Point out each Plasmodium parasite.
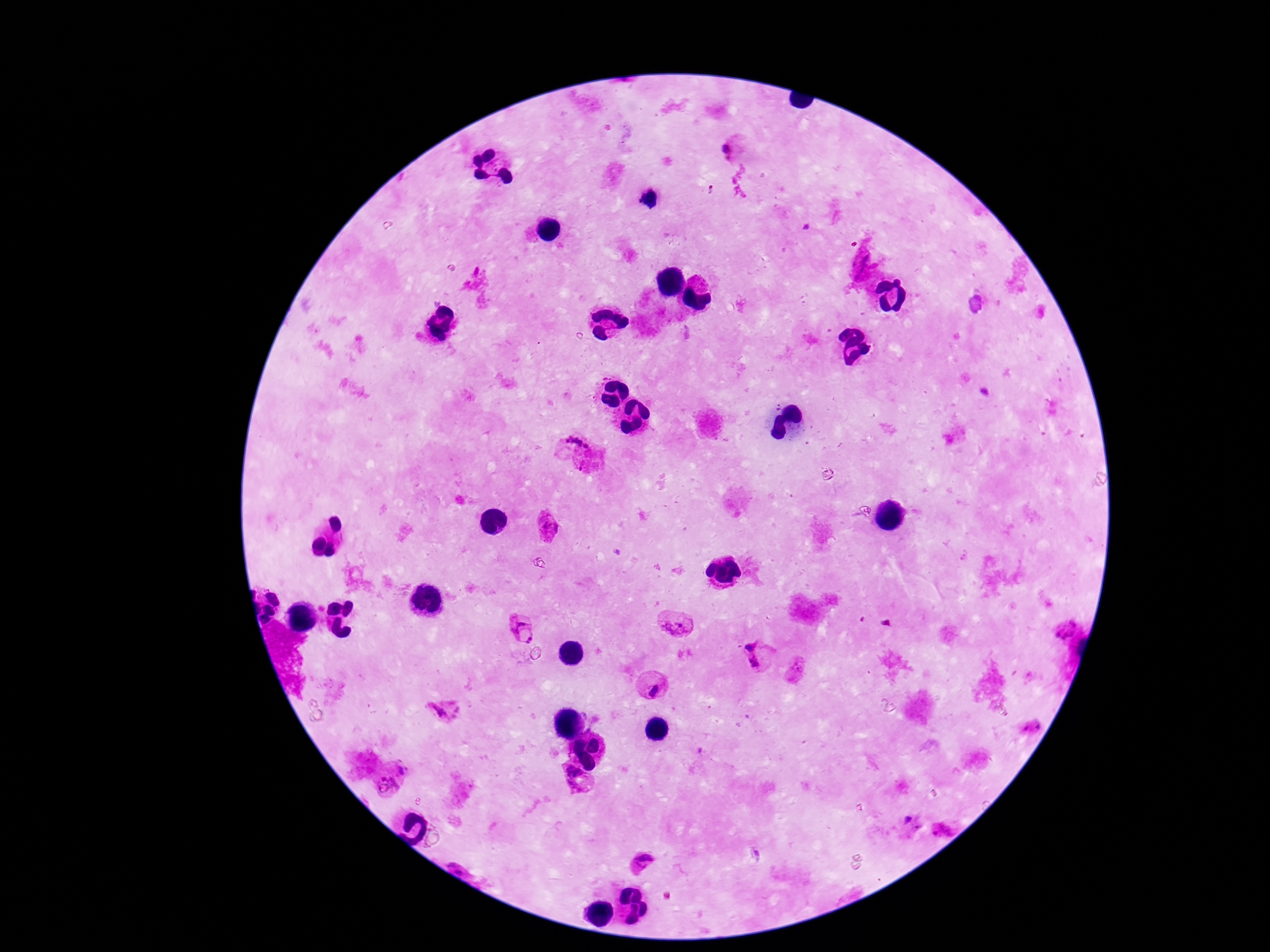
Approximate object centers, in pixels from the top-left corner.
Plasmodium parasites: (x=728, y=149), (x=571, y=438), (x=588, y=447), (x=546, y=527), (x=678, y=623), (x=522, y=629), (x=752, y=645), (x=755, y=661), (x=651, y=685), (x=442, y=711), (x=1033, y=727), (x=400, y=771), (x=574, y=780), (x=909, y=820), (x=944, y=829), (x=643, y=863).

field of view = single
capture = smartphone camera through the microscope eyepiece
magnification = 100x
patient malaria status = infected
preparation = thick blood smear
stain = Giemsa
image size = 1270×952 pixels